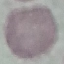

{
  "result": "negative for malaria parasites",
  "capture": "smartphone camera at the microscope eyepiece",
  "image_type": "cell patch, automatically extracted from a larger field of view and resized to 64 × 64 pixels",
  "stain": "Giemsa",
  "preparation": "thin blood film"
}